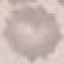

malaria_status: uninfected
image_type: cell patch, automatically extracted from a larger field of view and resized to 64 × 64 pixels
capture: smartphone camera at the microscope eyepiece
stain: Giemsa
preparation: thin smear